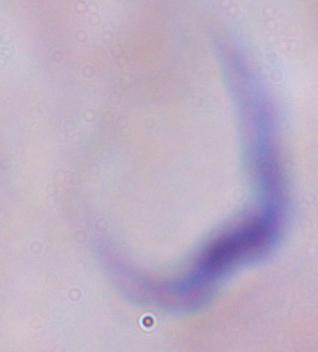

identification = trypanosome
modality = micrograph
magnification = 1000x